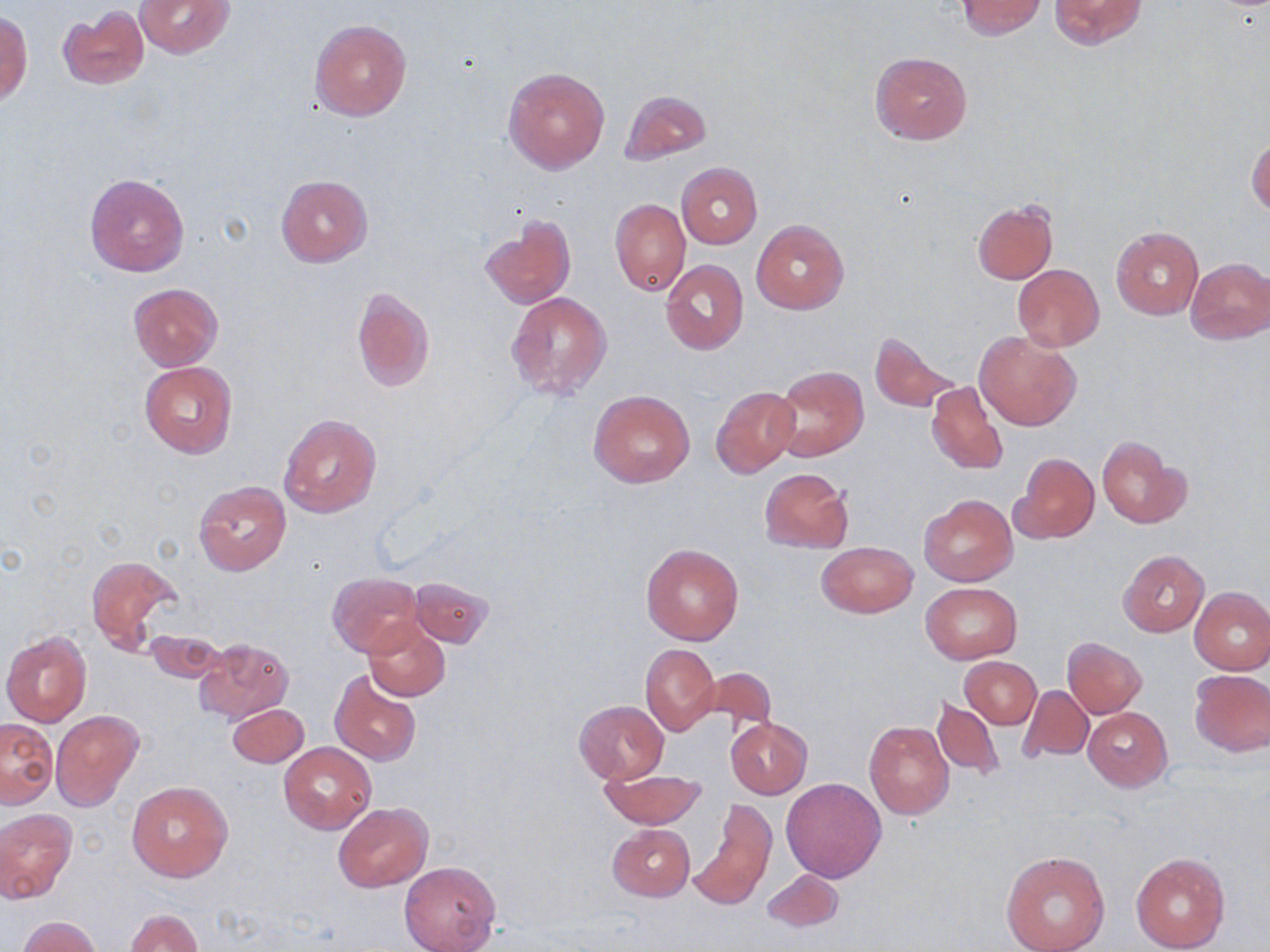

Approximate bounding boxes as (x1,y1)-(x2,y2) corner pairs in pixels. Uninfected red blood cell locations: (135,0)-(233,57), (956,0)-(1046,39), (1049,0)-(1146,49), (57,5)-(150,89), (0,11)-(33,104), (310,18)-(412,121), (869,52)-(972,145), (503,67)-(610,174), (620,89)-(710,166), (1247,133)-(1269,217), (676,162)-(761,249), (84,173)-(190,278), (276,174)-(373,267), (610,199)-(689,297), (974,199)-(1058,284), (479,215)-(576,310), (750,221)-(849,314), (1111,226)-(1204,319), (1184,258)-(1269,344), (660,259)-(748,355), (1012,264)-(1104,350), (130,283)-(223,371), (352,286)-(435,392), (506,291)-(611,400), (868,330)-(965,415), (975,330)-(1081,431), (139,361)-(237,458), (771,366)-(870,461), (926,381)-(1007,476), (711,385)-(800,478), (588,389)-(695,487), (277,414)-(381,518), (1097,434)-(1190,528), (1013,452)-(1099,543), (758,468)-(853,552), (193,480)-(291,576), (919,495)-(1017,585), (817,541)-(916,618), (641,544)-(744,645), (1118,549)-(1208,637), (87,555)-(182,655), (328,572)-(425,657), (408,577)-(493,646), (920,582)-(1022,663), (1189,587)-(1270,674), (363,617)-(452,702), (143,628)-(226,683), (2,631)-(92,728), (194,637)-(295,723), (1061,638)-(1147,718), (639,643)-(720,735), (960,657)-(1041,728), (696,667)-(777,738), (1189,669)-(1269,757), (330,670)-(422,767), (1018,686)-(1094,764), (930,695)-(1004,778), (574,701)-(669,783), (225,703)-(309,768), (1083,707)-(1172,789), (50,711)-(142,810), (724,716)-(812,799), (1,718)-(56,808), (864,721)-(954,819), (278,742)-(376,834), (601,765)-(703,829), (781,777)-(887,882), (127,780)-(233,881), (688,798)-(776,912), (333,803)-(432,892), (0,808)-(77,904), (607,823)-(695,901), (1000,849)-(1110,952), (1130,850)-(1230,951), (399,861)-(500,951), (759,868)-(843,933), (124,909)-(201,952), (18,916)-(104,952). Slide-level diagnosis: no evidence of blood parasites. Captured at 1000x magnification. Single field of view. Thin blood smear. Image is 1270×952 pixels. May-Grünwald-Giemsa stain. Light microscopy.